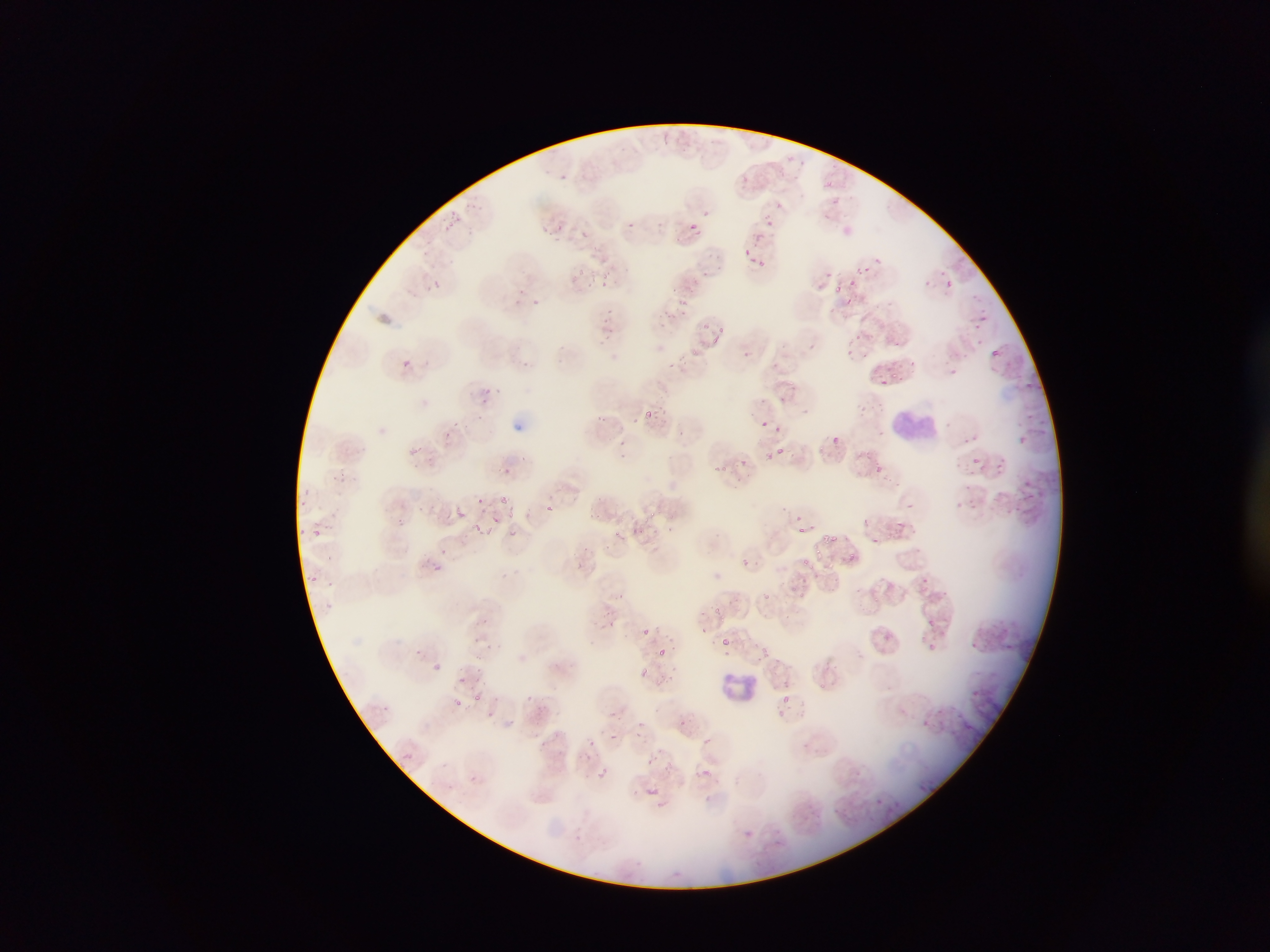 Approximate bounding boxes as left top right bottom in pixels. Malaria parasite locations: 557 172 569 183; 739 175 751 187; 622 216 640 232; 763 218 775 229; 557 219 570 231; 690 221 703 232; 584 224 600 244; 739 244 755 257; 708 252 721 264; 873 253 881 262; 756 259 769 274; 857 261 873 274; 577 267 587 280; 828 267 835 275; 686 269 700 281; 605 277 615 290; 848 277 858 287; 944 279 955 289; 429 280 441 291; 516 283 529 296; 832 283 849 295; 680 297 690 308; 843 297 860 309; 533 299 543 313; 977 309 996 321; 606 313 612 326; 701 318 709 329; 714 325 729 340; 851 327 862 341; 806 339 822 351; 845 341 864 357; 987 347 1003 361; 673 354 690 375; 888 356 904 370; 400 359 413 370; 949 362 962 376; 882 375 893 388; 1025 375 1037 387; 479 389 491 403; 642 405 667 420; 762 417 788 430; 449 421 459 431; 969 428 983 444; 444 431 450 444; 1017 432 1029 444; 832 434 845 444; 410 441 430 457; 970 450 981 466; 770 453 775 461; 741 456 752 469; 998 456 1010 467; 870 462 882 470; 502 466 515 472; 1024 474 1039 495; 961 491 981 517; 1003 492 1019 508; 498 495 508 504; 476 497 484 505; 911 502 922 510; 545 503 558 513; 333 505 344 518; 453 508 474 516; 391 509 404 522; 489 512 507 526; 794 514 803 523; 897 518 914 536; 473 519 487 530; 633 523 651 541; 505 527 519 537; 311 528 322 539; 819 532 839 547; 870 538 881 546; 793 549 814 567; 739 557 751 569; 428 563 458 576; 918 576 930 587; 790 580 812 596; 926 616 937 627; 641 627 651 637; 717 632 734 653; 920 634 933 652; 971 639 989 654; 1001 641 1017 655; 654 645 670 656; 642 668 661 685; 968 686 984 702; 447 694 468 714; 781 696 794 709; 675 716 691 732; 917 717 933 732; 399 748 416 764; 645 758 653 766; 696 764 714 780; 596 766 610 780; 468 773 481 785; 642 787 664 805 | approximate x y pixel centers of objects too small to bound: 778 449; 428 506. Leukocyte locations: 891 404 936 446; 716 669 765 711. Thin blood film. Image is 1270×952 pixels. Mobile-phone photograph taken through the microscope. Sample from Ghana. One field of view.